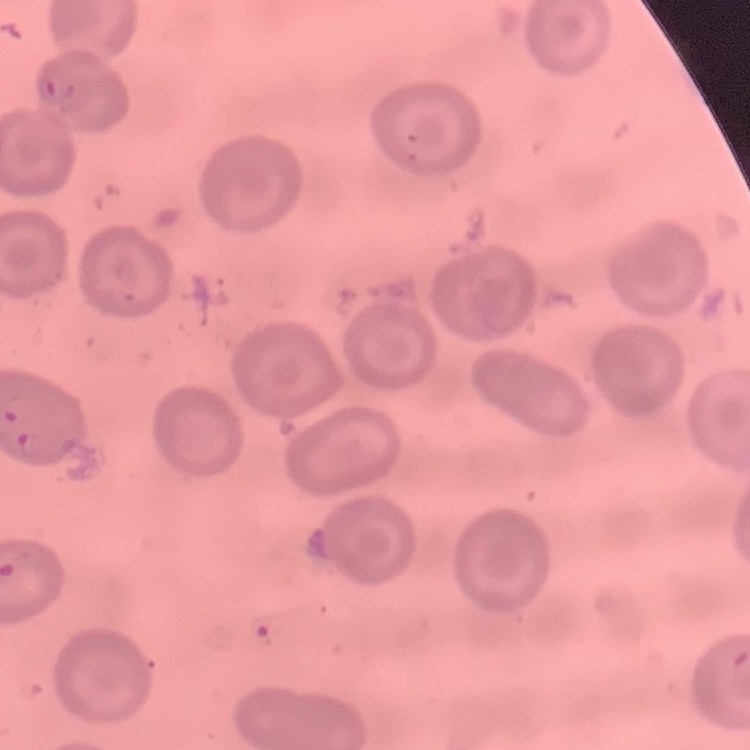 The erythrocytes show no rouleaux formation. Stained with either Field's or Giemsa. Square crop of a larger photomicrograph. Thin blood film.